Identify the parasite.
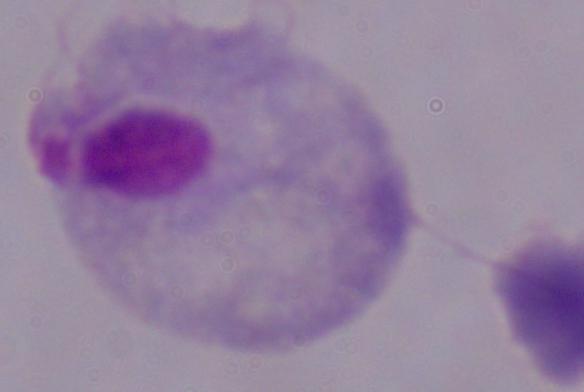
A trichomonad.

Summary:
  - Modality: micrograph
  - Magnification: 1000x